Locate every Plasmodium parasite.
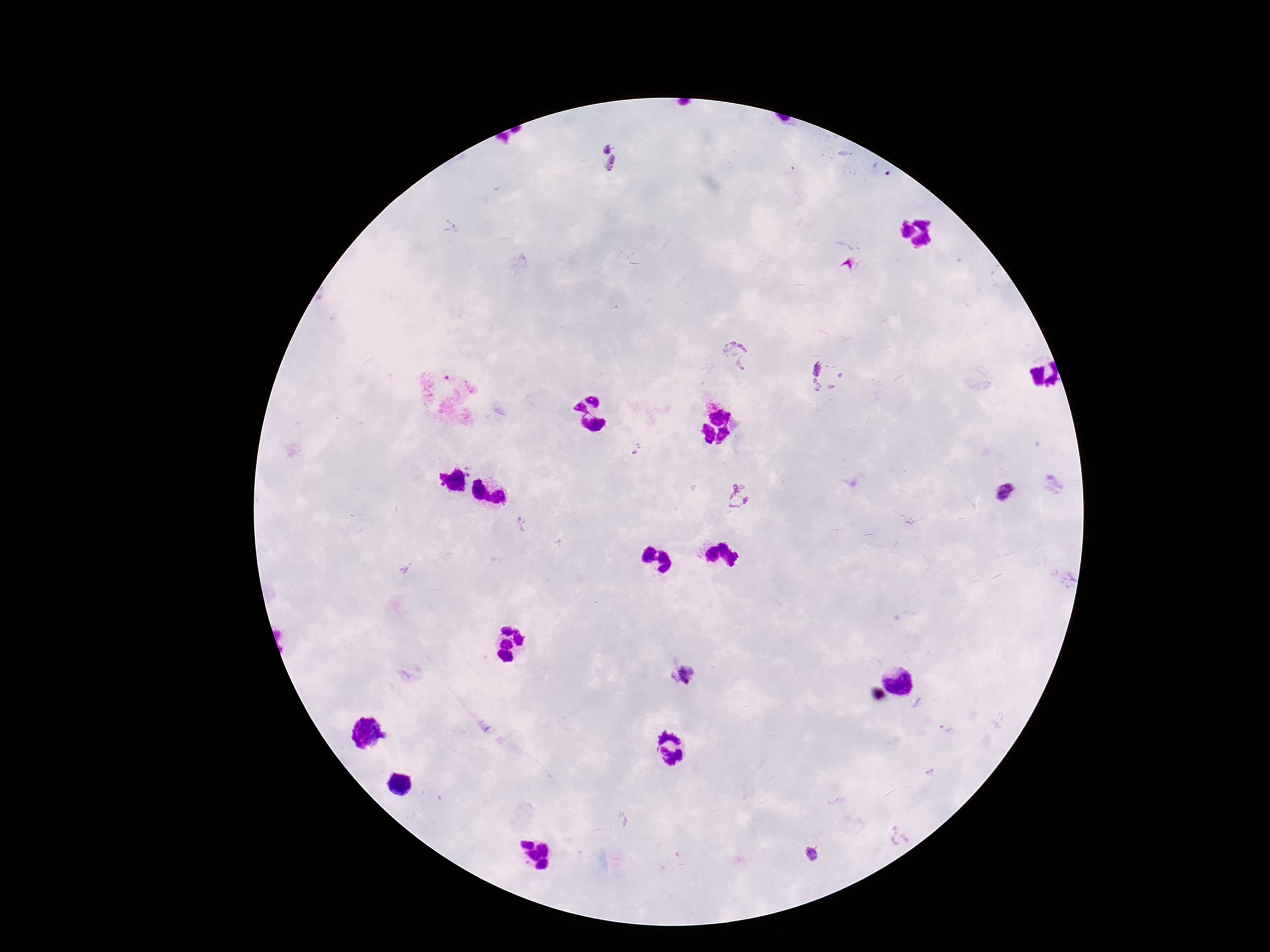

Approximate centers as (x, y) in pixels.
Plasmodium parasites: (607, 147), (613, 164), (451, 226), (737, 352), (824, 377), (636, 450), (1006, 491), (738, 498), (681, 673), (812, 854).

magnification = 100x
field of view = single
image size = 1270×952 pixels
capture = smartphone camera through the microscope eyepiece
preparation = thick blood smear
stain = Giemsa
patient malaria status = infected